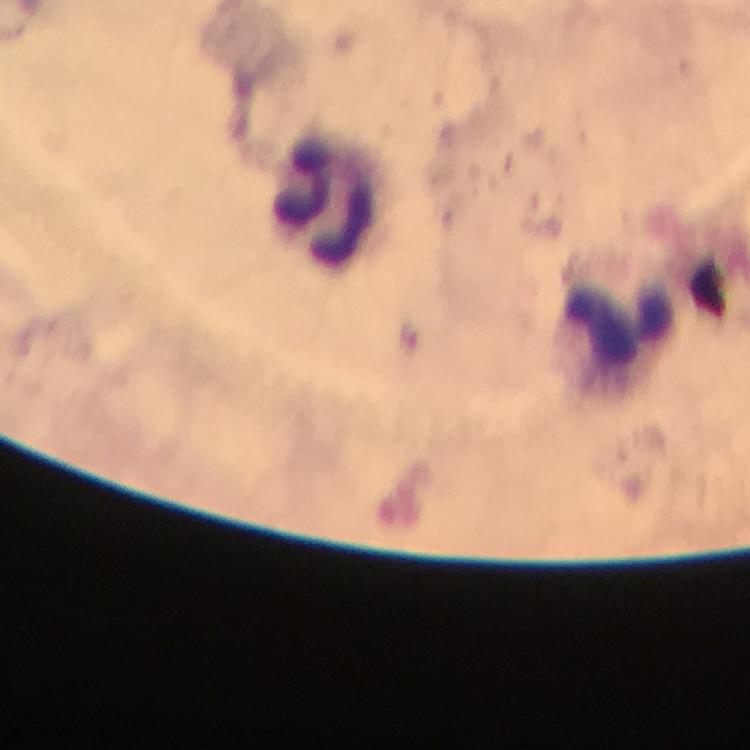

Approximate object centers, in pixels from the top-left corner. Leukocyte locations: (x=325, y=202), (x=622, y=327). Immersion oil was used. Smartphone photograph taken through a microscope. A crop from one field of view. Thick smear. Image is 750×750 pixels. At 100x magnification. From a diagnostic examination for malaria. Giemsa stain. Malaria parasites: none detected.